Locate every Plasmodium parasite.
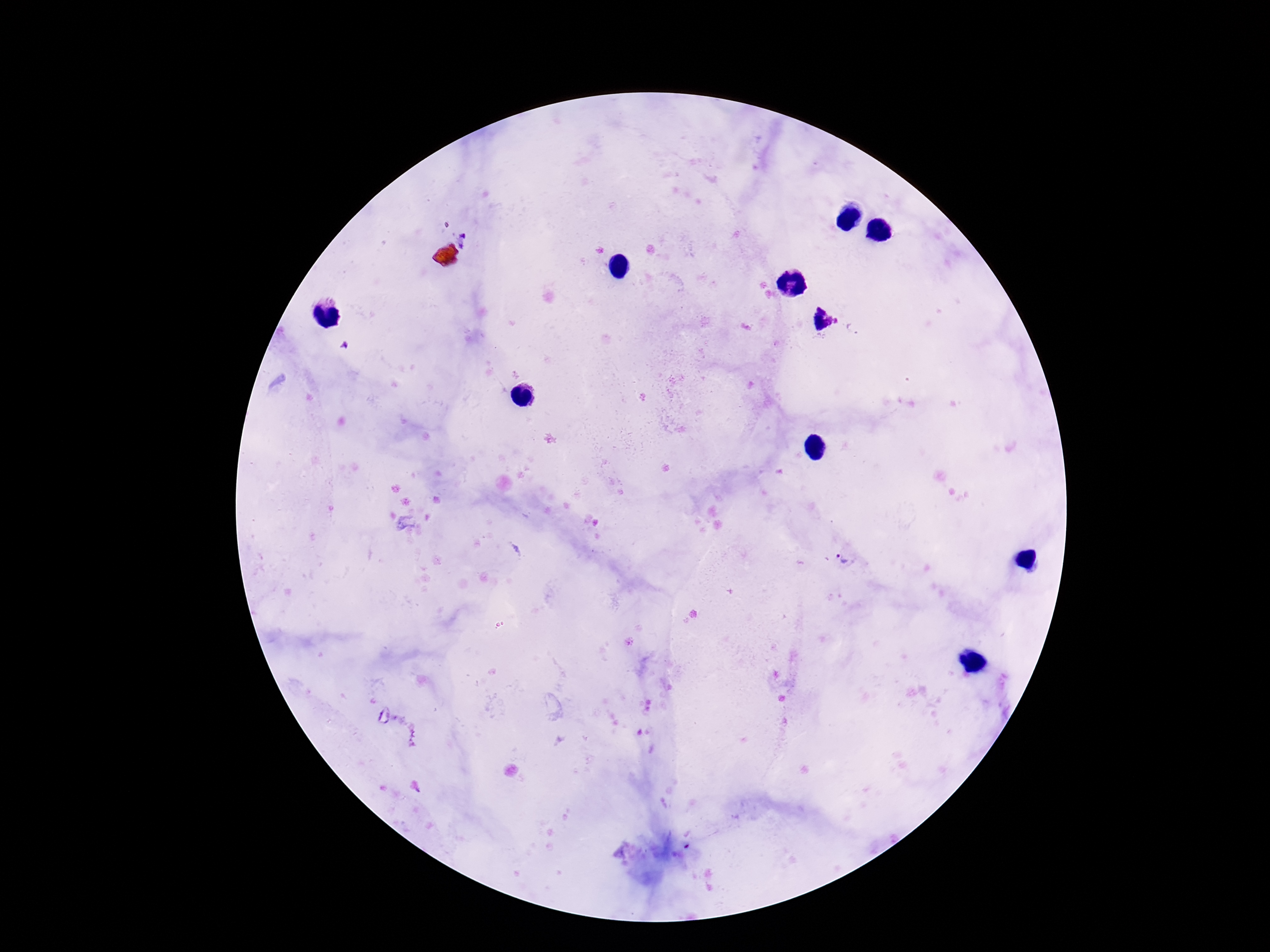
Approximate centers as {x, y} in pixels.
Plasmodium parasites: {466, 240}, {822, 320}, {845, 561}.

Giemsa-stained preparation. Photographed through the microscope eyepiece with a smartphone camera. 100x magnification. Single field of view. Image is 1270×952 pixels. Patient malaria status: positive. Thick blood smear.